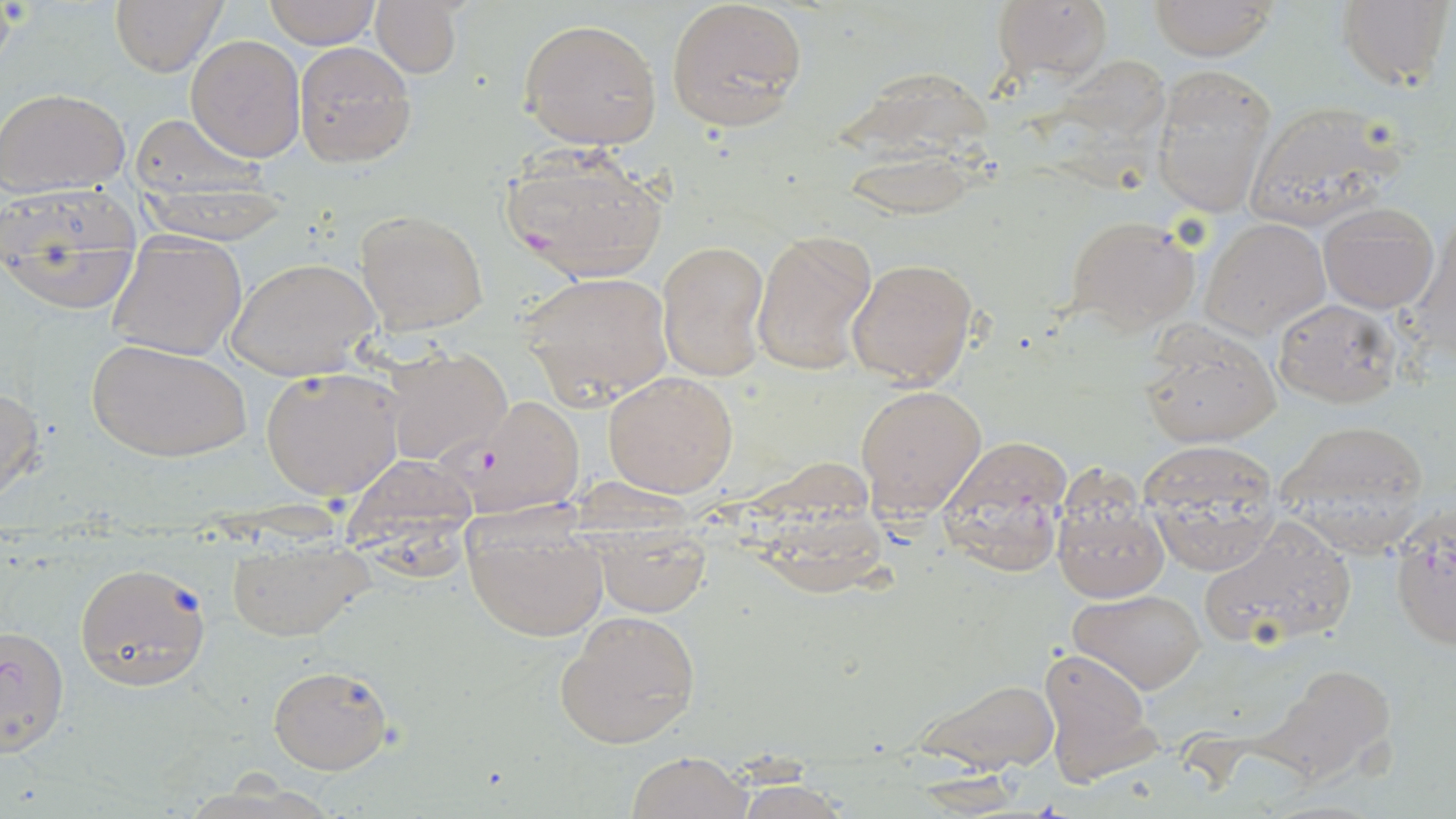

slide-level diagnosis = Plasmodium falciparum
uninfected red blood cell locations = approximate bounding boxes as named x1/y1/x2/y2 corners in pixels: (x1=263, y1=0, x2=380, y2=47), (x1=665, y1=0, x2=808, y2=132), (x1=989, y1=0, x2=1114, y2=87), (x1=1144, y1=0, x2=1281, y2=60), (x1=1336, y1=0, x2=1453, y2=91), (x1=109, y1=1, x2=225, y2=76), (x1=371, y1=1, x2=461, y2=77), (x1=518, y1=16, x2=664, y2=152), (x1=186, y1=35, x2=306, y2=160), (x1=292, y1=43, x2=414, y2=166), (x1=1030, y1=57, x2=1166, y2=200), (x1=1150, y1=64, x2=1277, y2=219), (x1=838, y1=66, x2=997, y2=219), (x1=0, y1=89, x2=130, y2=195), (x1=1241, y1=100, x2=1405, y2=230), (x1=125, y1=112, x2=275, y2=212), (x1=1, y1=178, x2=137, y2=310), (x1=1319, y1=200, x2=1439, y2=313), (x1=355, y1=209, x2=490, y2=336), (x1=1067, y1=216, x2=1201, y2=336), (x1=1202, y1=217, x2=1328, y2=338), (x1=752, y1=229, x2=877, y2=375), (x1=104, y1=232, x2=247, y2=359), (x1=658, y1=239, x2=770, y2=382), (x1=226, y1=256, x2=379, y2=380), (x1=847, y1=257, x2=979, y2=389), (x1=519, y1=270, x2=673, y2=408), (x1=1272, y1=297, x2=1403, y2=407), (x1=1138, y1=321, x2=1281, y2=448), (x1=88, y1=339, x2=251, y2=462), (x1=381, y1=345, x2=512, y2=466), (x1=259, y1=365, x2=406, y2=502), (x1=603, y1=371, x2=738, y2=498), (x1=0, y1=382, x2=45, y2=503), (x1=855, y1=383, x2=986, y2=517), (x1=1276, y1=421, x2=1432, y2=555), (x1=1138, y1=439, x2=1283, y2=574), (x1=338, y1=453, x2=479, y2=563), (x1=1052, y1=485, x2=1169, y2=602), (x1=461, y1=507, x2=608, y2=642), (x1=1389, y1=509, x2=1455, y2=651), (x1=1198, y1=514, x2=1359, y2=652), (x1=587, y1=521, x2=712, y2=614), (x1=225, y1=536, x2=373, y2=640), (x1=75, y1=562, x2=210, y2=691), (x1=1070, y1=589, x2=1206, y2=694), (x1=554, y1=609, x2=700, y2=749), (x1=0, y1=625, x2=68, y2=754), (x1=1037, y1=646, x2=1158, y2=785), (x1=1257, y1=660, x2=1399, y2=787), (x1=267, y1=663, x2=394, y2=775), (x1=909, y1=674, x2=1059, y2=774), (x1=626, y1=750, x2=752, y2=819), (x1=727, y1=781, x2=855, y2=819)
image size = 1456×819 pixels
preparation = thin blood film
magnification = 1000x
modality = optical microscopy
field of view = one of a larger specimen
Plasmodium falciparum-infected red blood cell locations = approximate bounding boxes as named x1/y1/x2/y2 corners in pixels: (x1=500, y1=144, x2=669, y2=281), (x1=449, y1=393, x2=585, y2=517), (x1=937, y1=440, x2=1071, y2=577)
stain = May-Grünwald-Giemsa